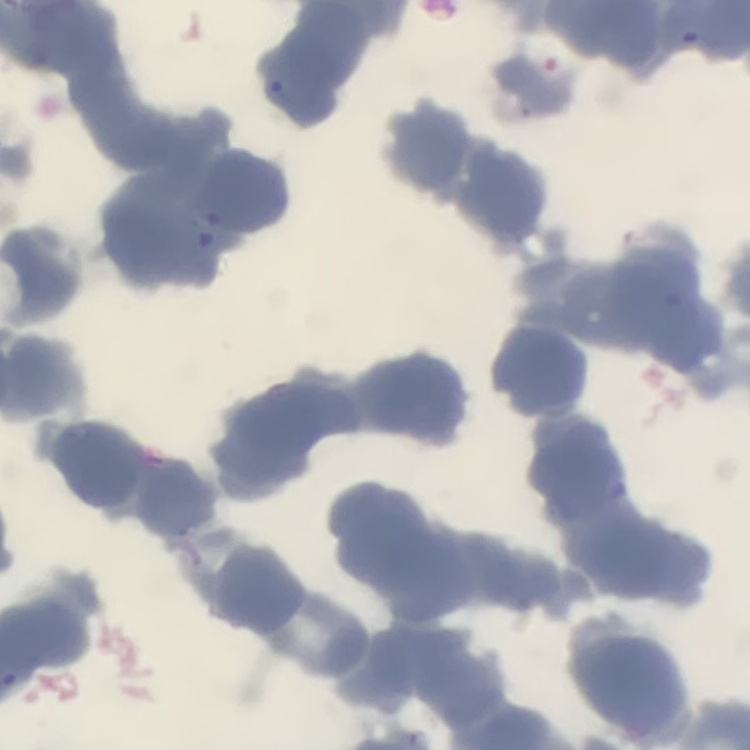

The erythrocytes show rouleaux formation. Field's or Giemsa stain. Thin peripheral smear. Square crop of a larger photomicrograph.